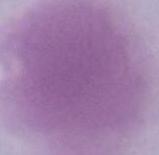

magnification = 1000x
identification = erythrocyte
modality = photomicrograph